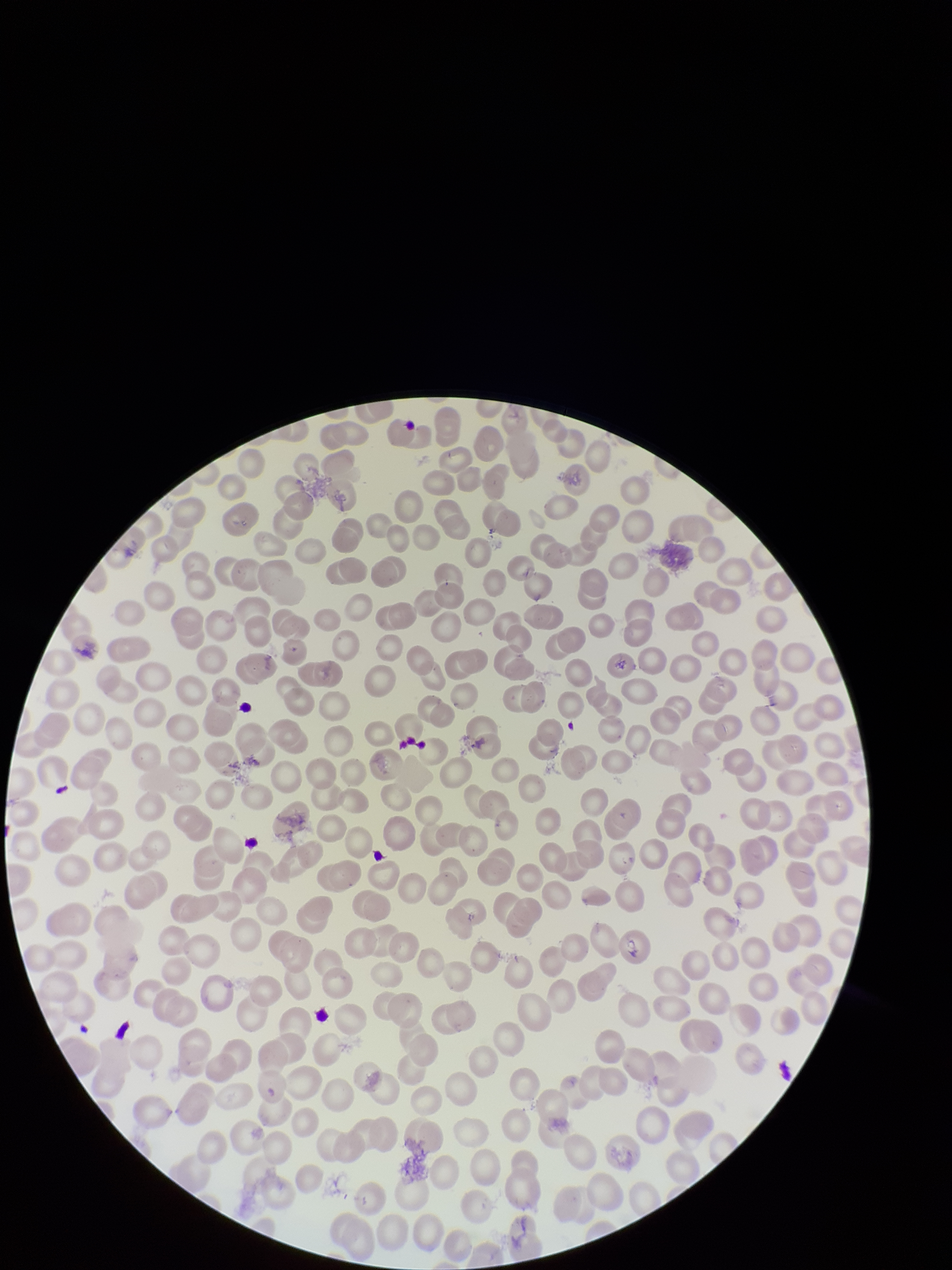

Summary:
  - Red blood cell count: 240
  - Image size: 952×1270 pixels
  - Stain: Giemsa
  - Field of view: single
  - Parasitized red blood cells: none detected
  - Capture: smartphone photograph through the microscope eyepiece
  - Preparation: thin smear
  - Patient malaria status: negative
  - Parasitized red blood cell count: 0